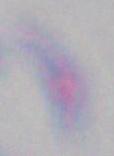

Summary:
  - Magnification: 1000x
  - Identification: Toxoplasma gondii
  - Modality: micrograph